Assess this cell for malaria.
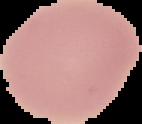

It is uninfected.

Summary:
  - Preparation: thin blood smear
  - Image type: segmented cell region on a black background
  - Image size: 142×124 pixels